Assess the morphology of the erythrocytes.
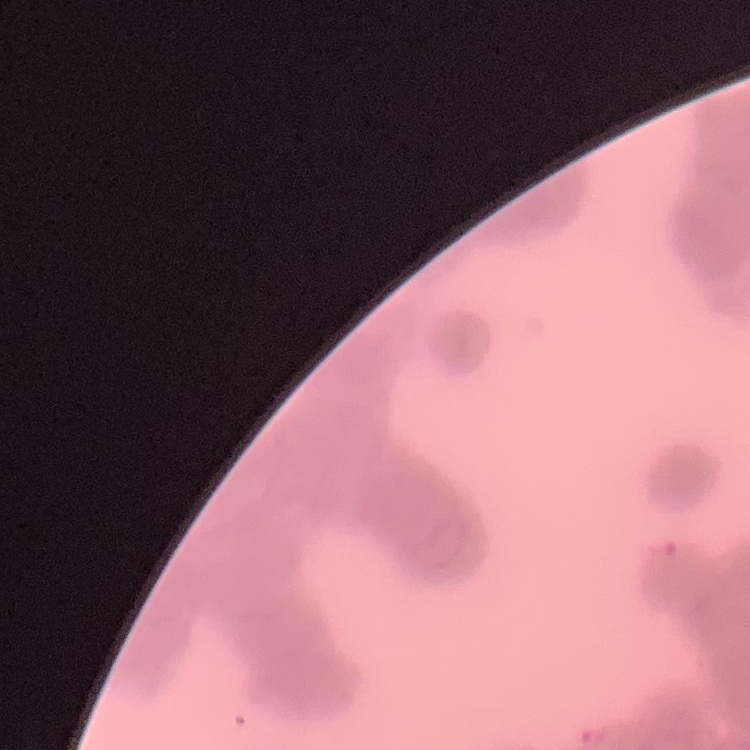

They show rouleaux formation.

Summary:
  - Stain: Field's or Giemsa
  - Preparation: thin blood smear
  - Image type: square crop of a larger photomicrograph